Report the malaria status of this cell.
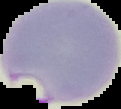
Parasitized.

image type = segmented cell region on a black background
preparation = thin blood smear
image size = 121×109 pixels